Classify this cell by malaria status.
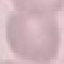
Uninfected.

image_type: cell patch, automatically extracted from a larger field of view and resized to 64 × 64 pixels
capture: smartphone through the microscope eyepiece
stain: Giemsa
preparation: thin smear